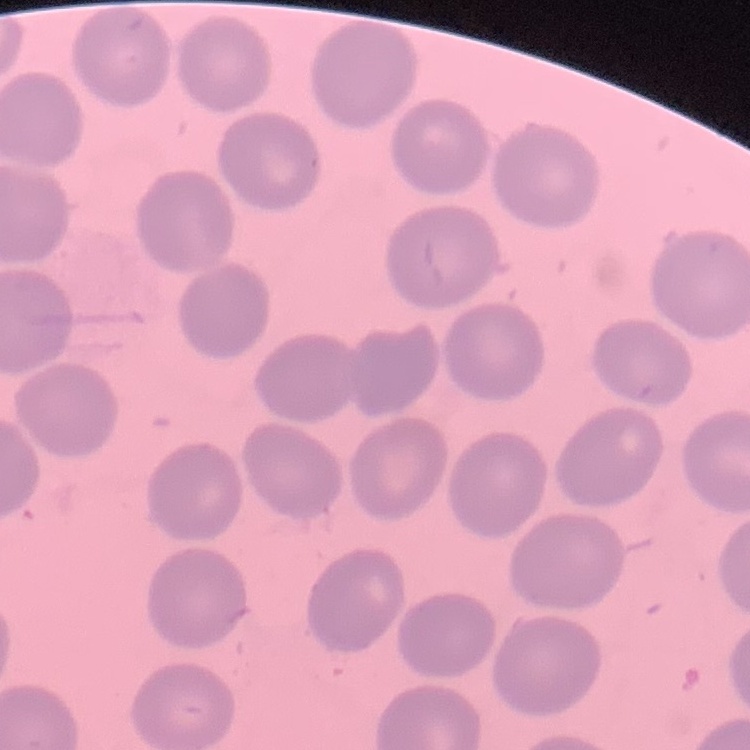

erythrocyte morphology = no rouleaux formation
stain = Field's or Giemsa
image type = square crop of a larger photomicrograph
preparation = thin blood film